Locate platelets.
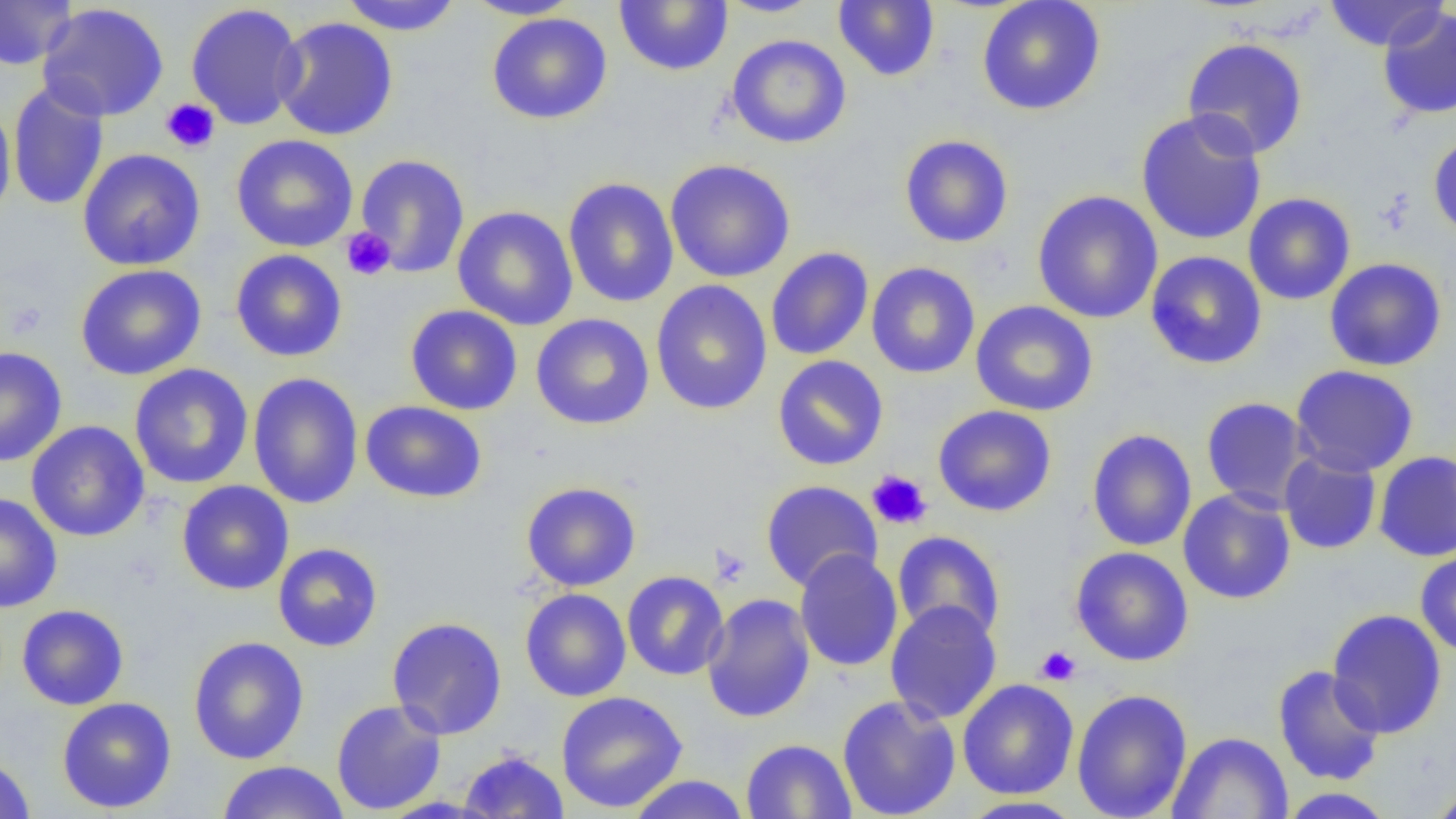

Approximate bounding boxes as [x1, y1, x2, y2] in pixels.
Platelets: [161, 98, 220, 153], [341, 227, 395, 281], [5, 301, 50, 340], [866, 469, 933, 530], [711, 545, 751, 586], [1035, 645, 1082, 686].

Summary:
  - Uninfected red blood cell locations: [0, 0, 78, 70], [463, 0, 580, 20], [716, 0, 824, 18], [976, 0, 1106, 116], [1322, 0, 1449, 51], [338, 1, 463, 35], [614, 1, 733, 75], [833, 1, 940, 82], [185, 2, 306, 130], [36, 3, 170, 122], [1378, 6, 1456, 120], [486, 12, 613, 125], [272, 17, 399, 141], [726, 34, 852, 149], [1182, 37, 1309, 159], [8, 82, 110, 211], [0, 102, 16, 225], [1135, 109, 1267, 246], [1428, 133, 1456, 241], [230, 134, 359, 252], [899, 134, 1014, 248], [77, 148, 206, 271], [354, 153, 470, 278], [665, 159, 796, 283], [563, 177, 679, 308], [1031, 190, 1163, 324], [1243, 193, 1356, 305], [452, 205, 579, 331], [765, 247, 874, 361], [230, 249, 347, 362], [1145, 250, 1267, 369], [1324, 257, 1447, 372], [866, 262, 980, 378], [76, 264, 207, 381], [649, 280, 773, 415], [971, 300, 1098, 416], [405, 305, 523, 415], [531, 313, 654, 430], [0, 346, 67, 466], [772, 355, 889, 470], [129, 363, 253, 489], [1290, 364, 1419, 477], [248, 372, 363, 510], [1201, 397, 1312, 511], [360, 400, 487, 503], [933, 404, 1058, 517], [26, 420, 150, 542], [1086, 429, 1196, 552], [1374, 450, 1456, 562], [1279, 451, 1382, 554], [177, 480, 294, 595], [760, 480, 883, 592], [521, 481, 640, 591], [1178, 488, 1296, 604], [0, 493, 63, 613], [892, 530, 1006, 642], [272, 543, 383, 652], [1070, 546, 1194, 667], [794, 549, 903, 672], [1415, 551, 1456, 657], [622, 570, 729, 681], [520, 588, 631, 701], [702, 593, 815, 723], [885, 600, 1002, 725], [16, 604, 129, 710], [1327, 609, 1448, 739], [386, 616, 508, 740], [188, 636, 309, 765], [1272, 665, 1385, 786], [957, 679, 1079, 799], [1071, 688, 1192, 819], [556, 691, 688, 813], [837, 694, 961, 818], [56, 697, 177, 814], [331, 700, 447, 816], [1167, 731, 1293, 819], [740, 739, 856, 818], [457, 749, 569, 818], [0, 754, 36, 818], [215, 760, 350, 819], [625, 774, 752, 819], [1426, 785, 1456, 818], [1278, 787, 1394, 818], [958, 796, 1086, 819]
  - Slide-level diagnosis: no evidence of blood parasites
  - Magnification: 1000x
  - Modality: optical microscopy
  - Image size: 1456×819 pixels
  - Field of view: one of a larger specimen
  - Preparation: thin blood film